Name the blood parasite species.
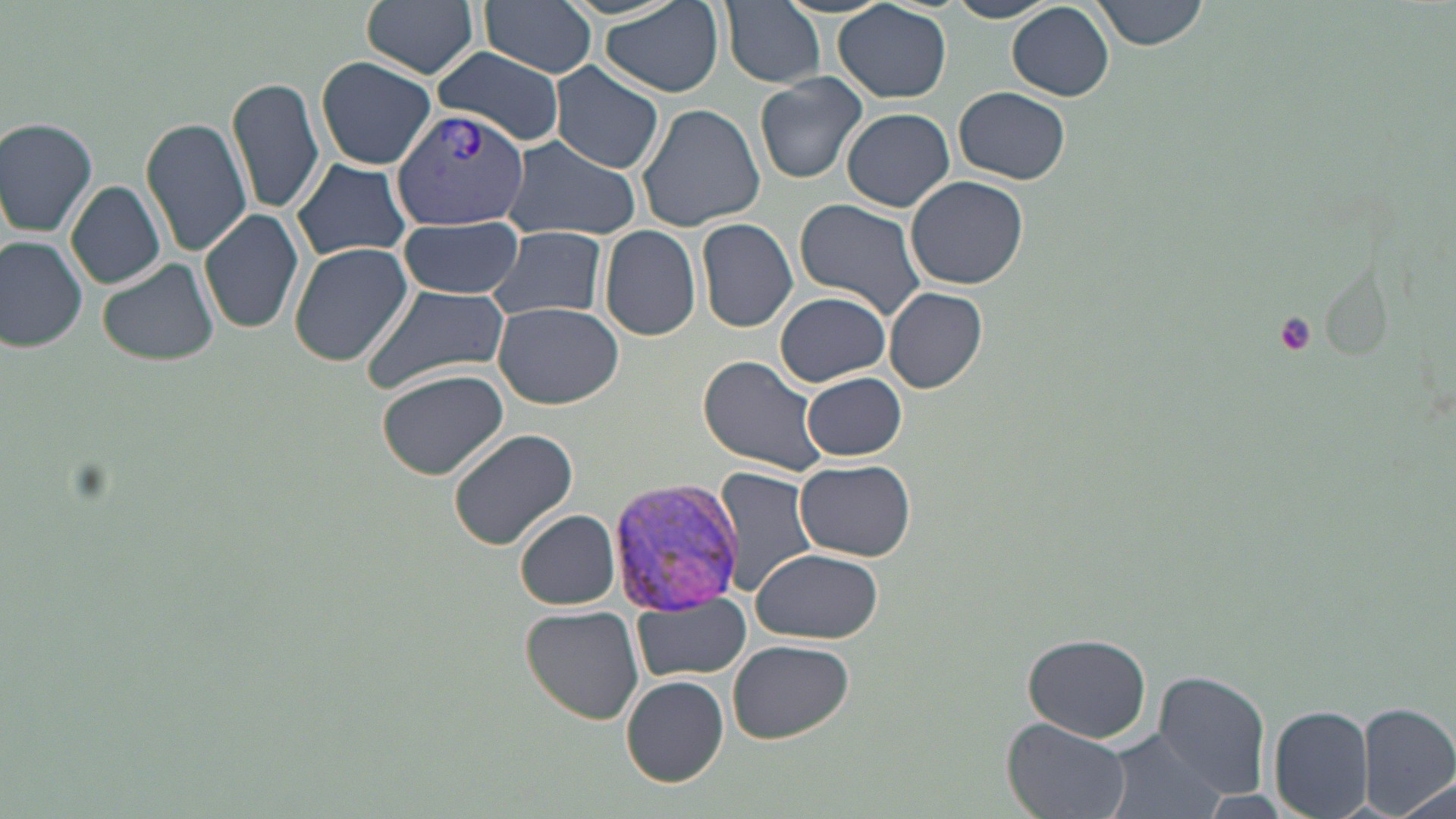

Plasmodium vivax.

Approximate bounding boxes as (x1,y1)-(x2,y2) corner pairs in pixels. Uninfected red blood cell locations: (362,0)-(481,80), (599,0)-(724,99), (721,0)-(825,88), (943,0)-(1057,23), (1091,0)-(1206,50), (478,1)-(598,81), (463,2)-(612,146), (835,3)-(951,104), (1007,3)-(1114,101), (432,49)-(567,145), (313,56)-(437,170), (550,64)-(664,173), (754,71)-(870,184), (228,74)-(325,217), (955,88)-(1070,184), (635,102)-(766,231), (842,108)-(954,211), (142,115)-(250,256), (0,116)-(99,236), (500,136)-(643,243), (291,156)-(412,262), (906,175)-(1029,290), (66,180)-(167,290), (795,200)-(928,319), (198,209)-(305,335), (398,216)-(524,296), (697,217)-(797,333), (487,225)-(609,321), (600,225)-(701,341), (0,234)-(89,350), (288,241)-(414,368), (97,254)-(220,367), (360,281)-(512,398), (884,287)-(988,395), (774,290)-(891,387), (493,302)-(625,408), (696,355)-(831,478), (375,369)-(508,480), (803,372)-(907,461), (446,428)-(582,553), (795,460)-(917,560), (715,466)-(823,597), (516,509)-(620,610), (750,548)-(883,643), (632,593)-(751,682), (519,607)-(644,724), (1023,632)-(1151,745), (729,639)-(854,742), (1153,670)-(1272,798), (621,675)-(730,786), (1355,702)-(1456,819), (1268,704)-(1374,818), (1002,717)-(1132,819), (1099,728)-(1227,819), (1386,776)-(1453,819). Platelet locations: (1272,312)-(1317,356). Plasmodium vivax-infected red blood cell locations: (393,105)-(531,228), (608,475)-(748,616). Optical microscopy. Single field of view. 1000x magnification. Image is 1456×819 pixels. Thin blood smear. May-Grünwald-Giemsa stain.